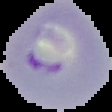

Image is 112×112 pixels. From a thin blood film. Result: Plasmodium parasites identified. Segmented cell region on a black background.